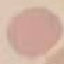
result = no malaria parasites seen
image type = cell patch, automatically extracted from a larger field of view and resized to 64 × 64 pixels
stain = Giemsa
capture = smartphone camera at the microscope eyepiece
preparation = thin smear